Comment on the morphology of the red blood cells.
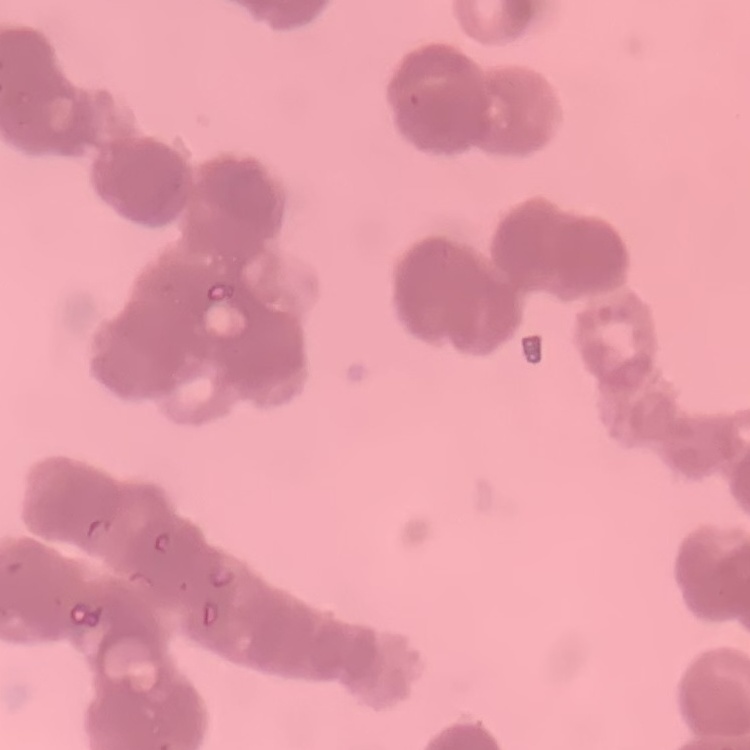

They show rouleaux formation.

Summary:
  - Stain: Field's or Giemsa
  - Image type: one tile cut from a larger photomicrograph
  - Preparation: thin blood smear